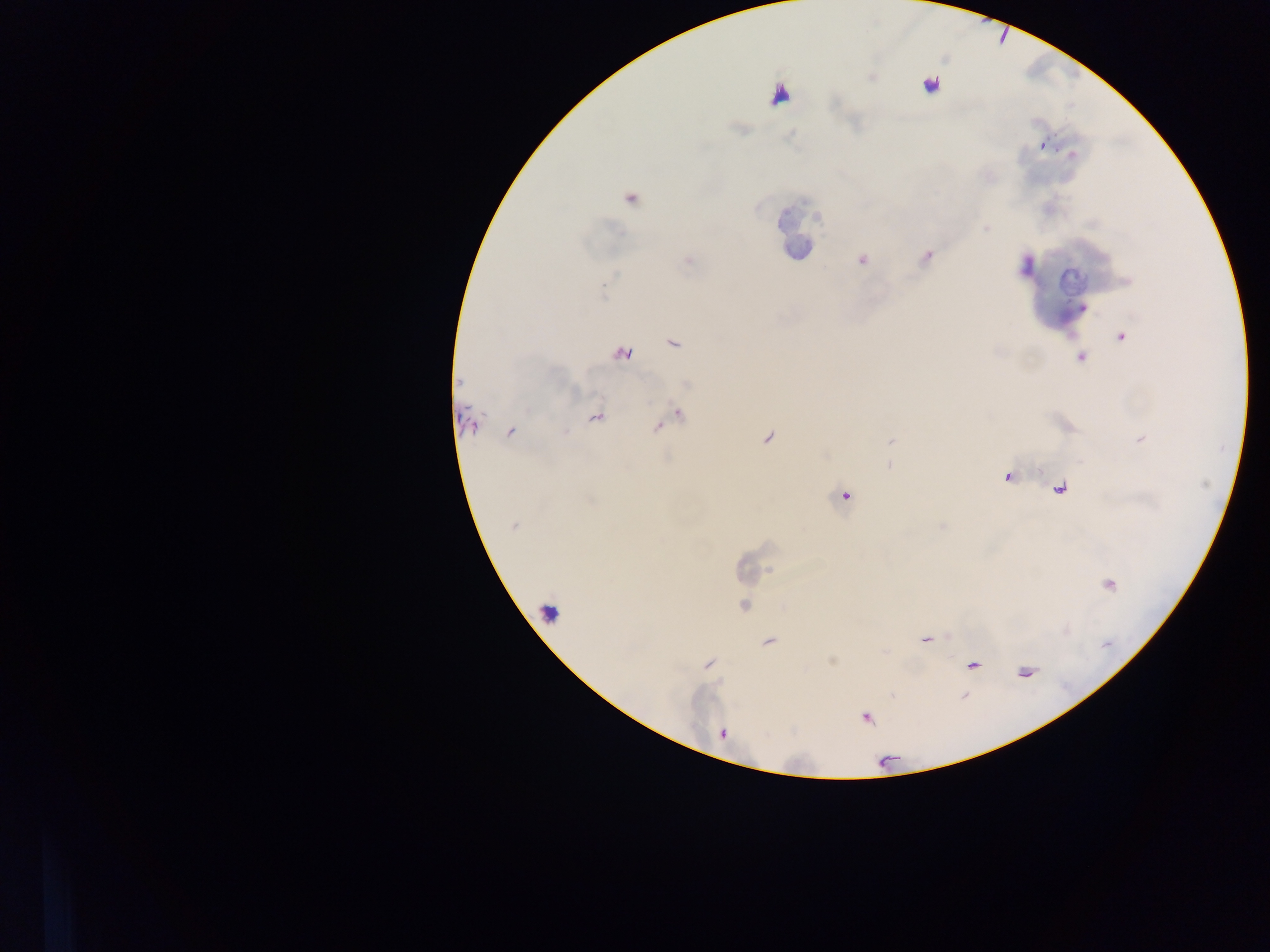 Approximate centers as [x, y] in pixels. Malaria parasite locations: [931, 85], [745, 130], [1043, 147], [1072, 153], [630, 197], [987, 229], [927, 256], [862, 260], [1083, 307], [1122, 337], [1082, 357], [679, 413], [656, 427], [566, 432], [890, 440], [888, 465], [846, 496], [514, 527], [770, 569], [719, 680], [869, 717]. Image is 1270×952 pixels. Mobile-phone photograph taken through the microscope. Single field of view. Sample from Ghana. Thick blood smear.